Name the blood parasite species.
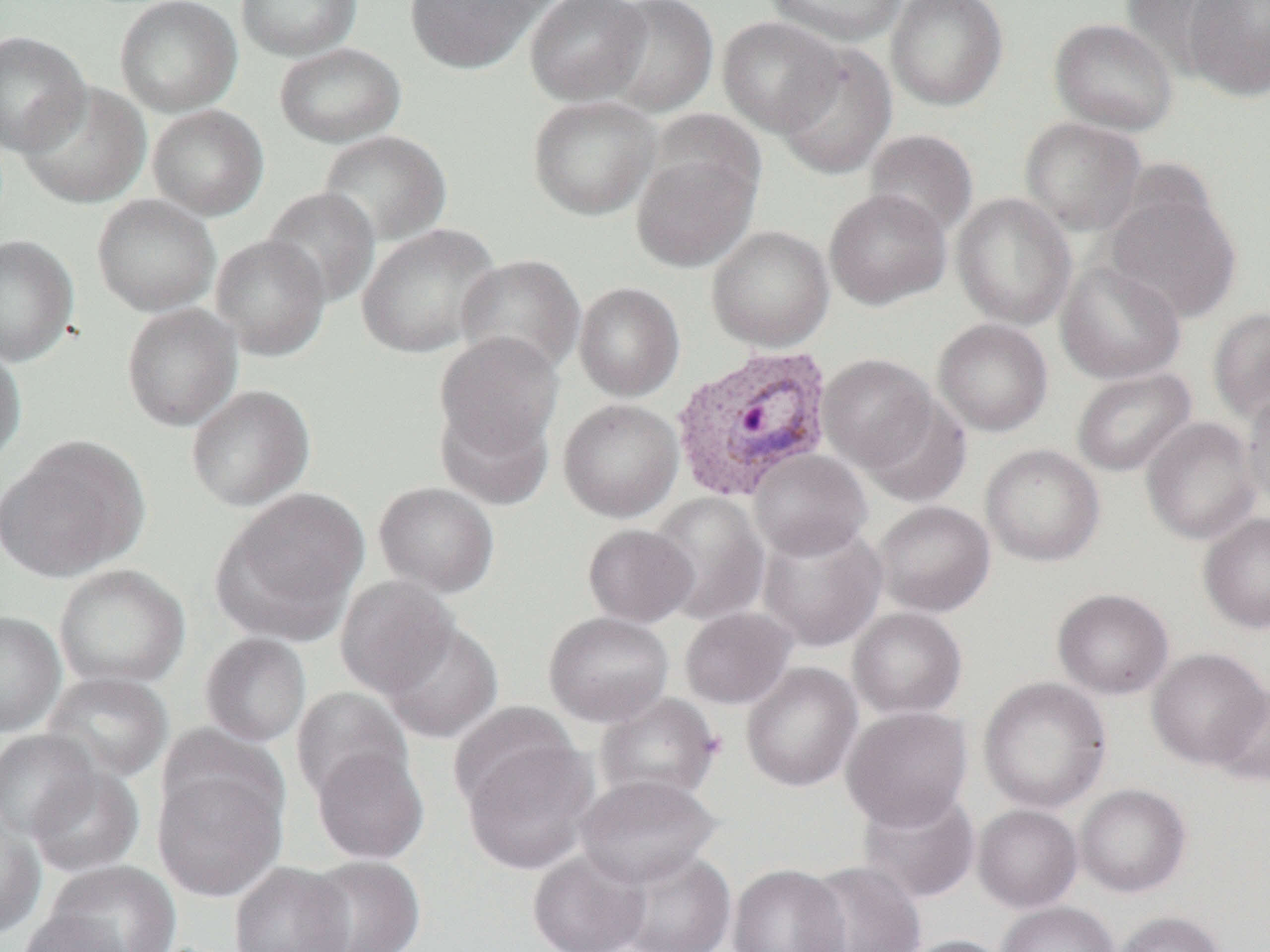
Plasmodium vivax.

Summary:
  - Coordinate format: approximate bounding boxes as [x1, y1, x2, y2] in pixels
  - Plasmodium vivax-infected red blood cell locations: [669, 344, 836, 501]
  - Uninfected red blood cell locations: [114, 0, 242, 116], [235, 0, 362, 61], [404, 0, 546, 74], [524, 0, 651, 107], [601, 0, 719, 118], [764, 0, 907, 47], [886, 0, 1009, 110], [1118, 0, 1243, 80], [1185, 1, 1270, 101], [716, 16, 843, 137], [1049, 17, 1179, 135], [0, 30, 91, 156], [274, 42, 406, 147], [774, 43, 897, 180], [18, 83, 151, 208], [527, 95, 662, 221], [147, 105, 269, 220], [647, 108, 767, 212], [1020, 117, 1147, 236], [863, 129, 979, 239], [317, 130, 452, 247], [630, 148, 760, 272], [261, 186, 381, 308], [1102, 186, 1241, 323], [824, 188, 951, 310], [951, 192, 1077, 329], [91, 194, 221, 317], [355, 223, 502, 359], [706, 225, 834, 352], [0, 234, 79, 366], [209, 234, 331, 361], [454, 254, 586, 377], [1055, 259, 1186, 384], [574, 282, 685, 402], [121, 302, 243, 432], [1208, 308, 1270, 424], [933, 318, 1053, 436], [434, 333, 564, 462], [0, 344, 27, 468], [817, 354, 939, 473], [1071, 367, 1196, 477], [185, 384, 316, 511], [1241, 389, 1270, 509], [859, 394, 971, 507], [558, 398, 683, 522], [435, 399, 555, 510], [1141, 417, 1262, 545], [0, 435, 149, 583], [980, 444, 1105, 567], [748, 448, 872, 560], [374, 481, 499, 598], [213, 487, 369, 641], [648, 492, 770, 625], [873, 500, 995, 617], [1199, 512, 1270, 634], [756, 520, 887, 652], [582, 523, 697, 627], [53, 564, 190, 690], [334, 576, 459, 699], [1052, 588, 1174, 699], [679, 606, 797, 709], [847, 607, 968, 719], [0, 610, 66, 737], [542, 611, 675, 727], [381, 620, 503, 743], [199, 632, 312, 747], [1146, 647, 1269, 769], [741, 662, 863, 792], [41, 671, 174, 783], [978, 676, 1112, 814], [1210, 684, 1270, 786], [291, 686, 412, 801], [595, 692, 723, 804], [449, 701, 578, 810], [841, 705, 973, 830], [157, 724, 289, 835], [0, 729, 100, 840], [461, 740, 598, 875], [311, 746, 429, 865], [152, 765, 287, 903], [27, 766, 144, 877], [575, 773, 723, 887], [1075, 783, 1191, 897], [856, 787, 981, 906], [972, 804, 1083, 912], [0, 816, 46, 939], [527, 848, 650, 952], [613, 848, 737, 952], [301, 855, 426, 952], [45, 860, 182, 952], [228, 861, 355, 952], [800, 861, 926, 952], [727, 864, 850, 952], [997, 901, 1119, 952], [15, 909, 136, 952], [1113, 910, 1226, 952], [896, 935, 1013, 952]
  - Image size: 1270×952 pixels
  - Preparation: thin blood film
  - Magnification: 1000x
  - Modality: optical microscopy
  - Field of view: single